Classify this cell by malaria status.
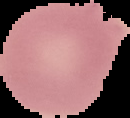
Uninfected.

Cell region segmented out of the field of view; the surrounding area is masked to black. Image is 130×118 pixels. From a thin blood smear.